Name the parasite shown.
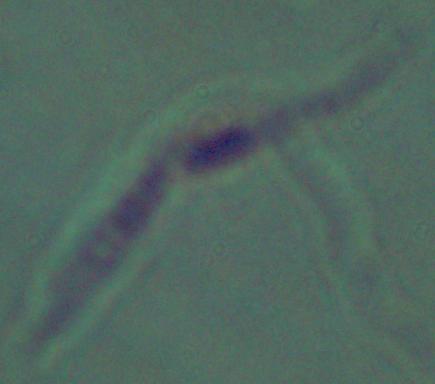

Leishmania.

modality = photomicrograph
magnification = 1000x